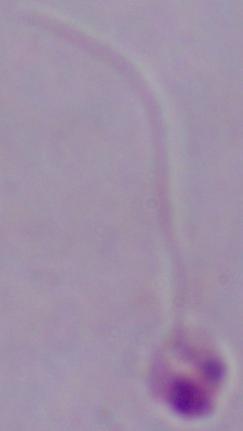
magnification = 1000x
modality = micrograph
identification = Leishmania